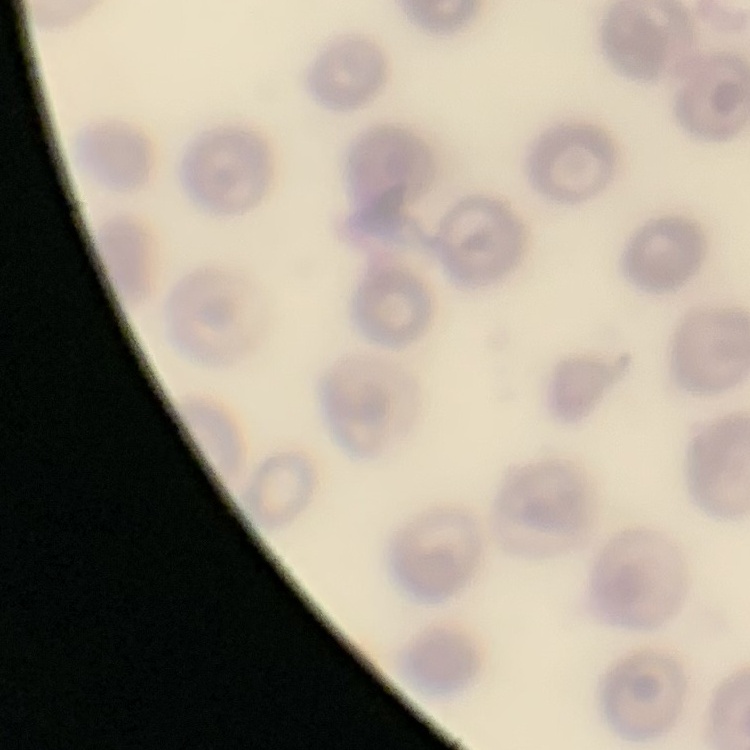

The erythrocytes exhibit no rouleaux formation. Field's or Giemsa stain. Thin blood film. One tile cut from a larger photomicrograph.